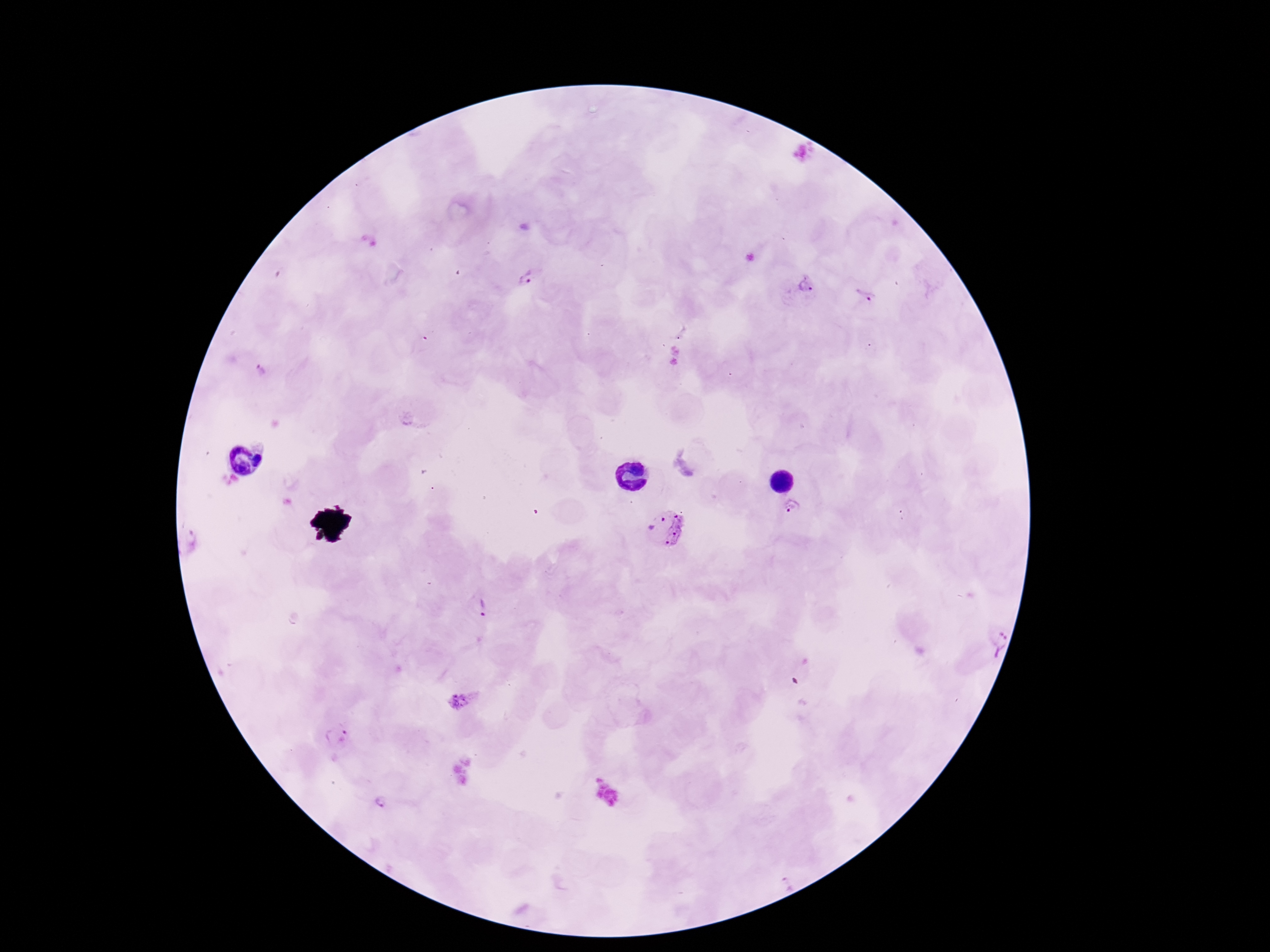
{
  "stain": "Giemsa",
  "image_size": "1270×952 pixels",
  "magnification": "100x",
  "field_of_view": "one from this slide",
  "plasmodium_parasite_locations": "approximate object centers, in pixels from the top-left corner: (x=527, y=278), (x=802, y=286), (x=867, y=294), (x=261, y=371), (x=794, y=506), (x=664, y=528), (x=474, y=608), (x=986, y=635), (x=463, y=700), (x=336, y=736), (x=381, y=800), (x=787, y=884)",
  "preparation": "thick blood film",
  "capture": "smartphone camera through the microscope eyepiece",
  "patient_malaria_status": "positive"
}